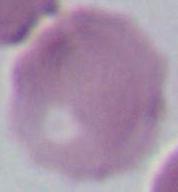

{
  "magnification": "1000x",
  "modality": "photomicrograph",
  "identification": "erythrocyte"
}